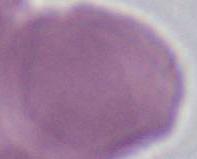
identification = red blood cell
magnification = 1000x
modality = micrograph